Report the malaria status.
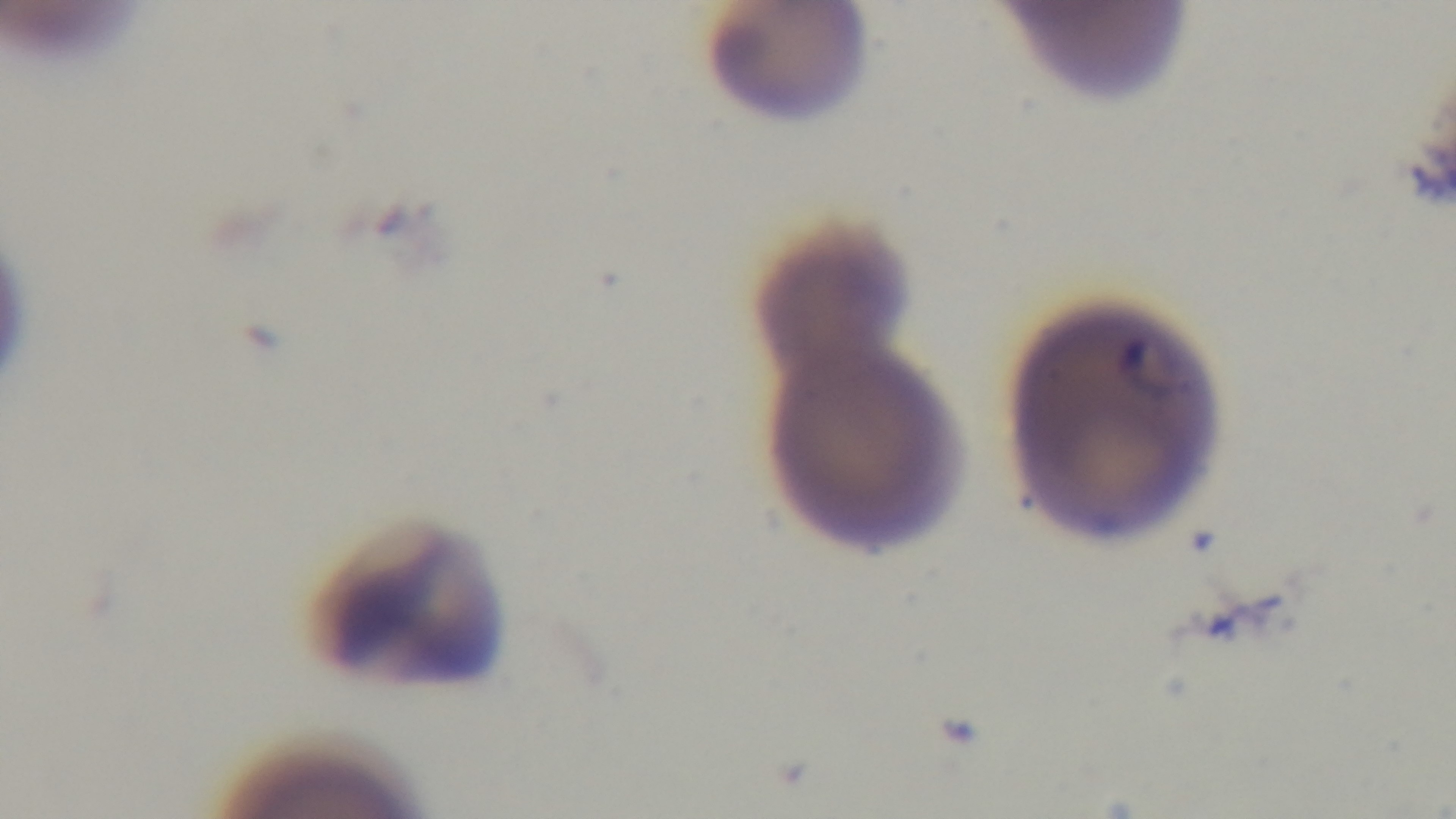

It is infected.

Giemsa stain. Mounted 4K digital camera. Light microscopy. Preparation: thin blood film. Single field of view. 100x oil-immersion objective.